Locate every blood parasite and identify its species.
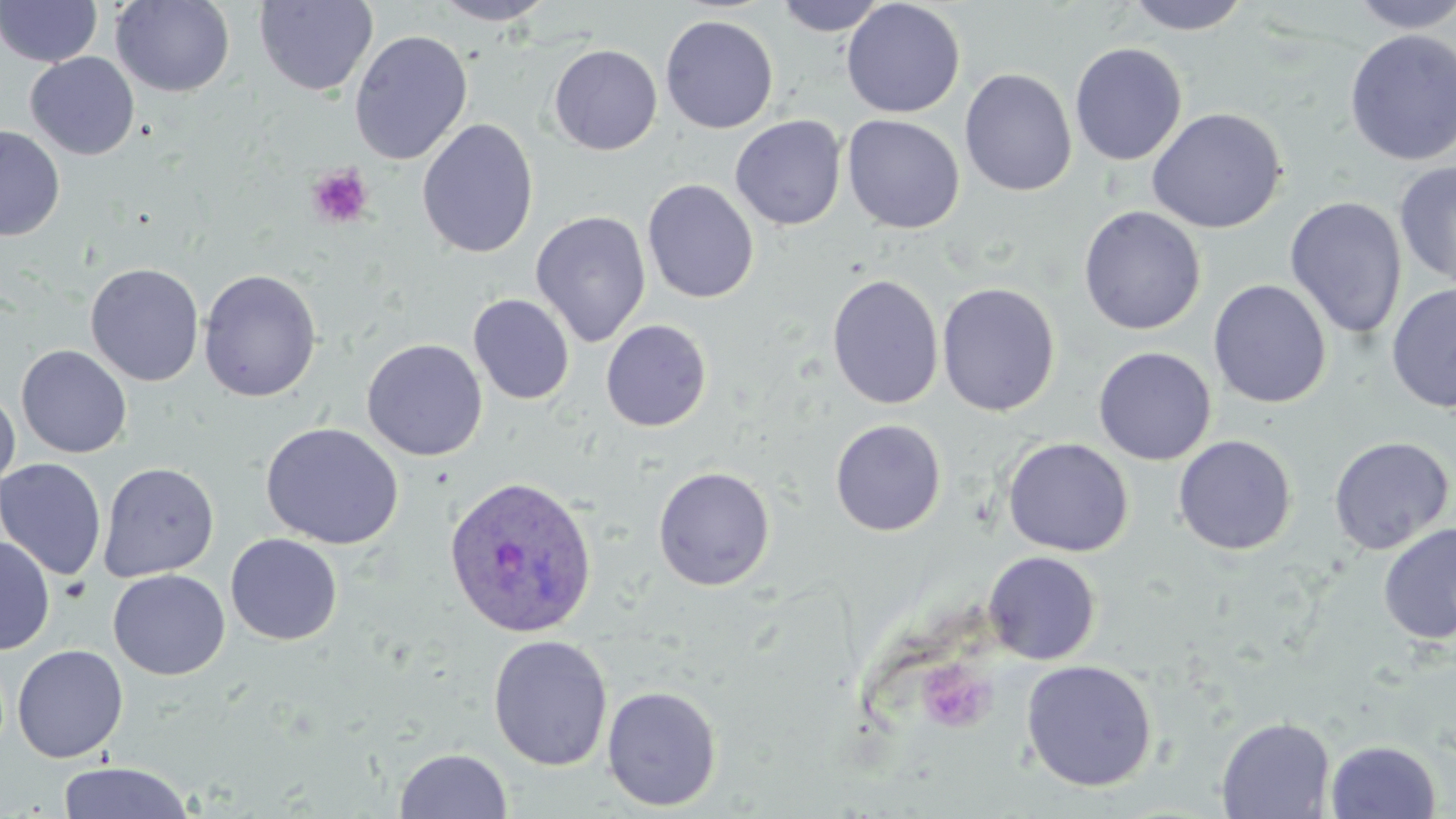

Approximate bounding boxes as named x1/y1/x2/y2 corners in pixels.
Plasmodium ovale-infected red blood cells: (x1=443, y1=474, x2=599, y2=638).
No Plasmodium falciparum, Plasmodium malariae, Plasmodium vivax, Babesia divergens, or Trypanosoma brucei observed.

Summary:
  - Platelet locations: (x1=306, y1=164, x2=373, y2=229), (x1=916, y1=659, x2=996, y2=734)
  - Uninfected red blood cell locations: (x1=110, y1=0, x2=235, y2=97), (x1=254, y1=0, x2=379, y2=96), (x1=431, y1=0, x2=557, y2=26), (x1=774, y1=0, x2=890, y2=35), (x1=841, y1=0, x2=966, y2=118), (x1=1122, y1=0, x2=1253, y2=34), (x1=1346, y1=0, x2=1456, y2=33), (x1=0, y1=1, x2=102, y2=66), (x1=660, y1=15, x2=779, y2=134), (x1=1343, y1=28, x2=1456, y2=166), (x1=350, y1=30, x2=473, y2=165), (x1=1068, y1=42, x2=1187, y2=165), (x1=548, y1=44, x2=662, y2=155), (x1=25, y1=53, x2=139, y2=160), (x1=959, y1=68, x2=1077, y2=197), (x1=1147, y1=107, x2=1287, y2=234), (x1=842, y1=114, x2=965, y2=234), (x1=730, y1=115, x2=846, y2=231), (x1=417, y1=118, x2=539, y2=259), (x1=0, y1=125, x2=65, y2=242), (x1=1394, y1=160, x2=1456, y2=289), (x1=642, y1=179, x2=759, y2=304), (x1=1285, y1=196, x2=1408, y2=340), (x1=1078, y1=205, x2=1206, y2=335), (x1=530, y1=210, x2=651, y2=347), (x1=85, y1=263, x2=204, y2=386), (x1=198, y1=268, x2=321, y2=402), (x1=826, y1=274, x2=944, y2=409), (x1=1208, y1=279, x2=1332, y2=408), (x1=937, y1=283, x2=1060, y2=416), (x1=1385, y1=283, x2=1456, y2=414), (x1=468, y1=294, x2=575, y2=405), (x1=600, y1=319, x2=713, y2=432), (x1=362, y1=338, x2=488, y2=461), (x1=16, y1=344, x2=132, y2=458), (x1=1093, y1=346, x2=1217, y2=465), (x1=0, y1=387, x2=20, y2=491), (x1=829, y1=419, x2=947, y2=536), (x1=260, y1=422, x2=404, y2=550), (x1=1173, y1=435, x2=1297, y2=555), (x1=1327, y1=435, x2=1454, y2=555), (x1=1002, y1=437, x2=1134, y2=557), (x1=0, y1=458, x2=107, y2=581), (x1=98, y1=462, x2=219, y2=582), (x1=652, y1=465, x2=776, y2=591), (x1=1378, y1=522, x2=1455, y2=646), (x1=225, y1=534, x2=343, y2=645), (x1=0, y1=535, x2=55, y2=655), (x1=983, y1=551, x2=1101, y2=665), (x1=108, y1=569, x2=230, y2=679), (x1=487, y1=634, x2=613, y2=771), (x1=12, y1=644, x2=128, y2=762), (x1=1020, y1=659, x2=1158, y2=792), (x1=602, y1=685, x2=722, y2=812), (x1=1216, y1=717, x2=1335, y2=818), (x1=1326, y1=740, x2=1442, y2=819), (x1=394, y1=748, x2=513, y2=818), (x1=56, y1=761, x2=195, y2=819)
  - Slide-level diagnosis: Plasmodium ovale
  - Field of view: one of a larger specimen
  - Preparation: thin blood smear
  - Modality: light microscopy
  - Image size: 1456×819 pixels
  - Magnification: 1000x
  - Stain: May-Grünwald-Giemsa